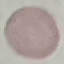
Summary:
  - Malaria status: uninfected
  - Capture: smartphone through the microscope eyepiece
  - Image type: automatically extracted cell patch, resized to 64 × 64 pixels
  - Preparation: thin blood film
  - Stain: Giemsa